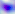

{
  "identification": "Toxoplasma gondii",
  "magnification": "400x",
  "modality": "photomicrograph"
}